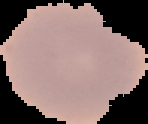

Summary:
  - Malaria status: uninfected
  - Preparation: thin blood film
  - Image type: cell region segmented out of the field of view; surrounding area masked to black
  - Image size: 148×124 pixels